Describe the morphology of the erythrocytes.
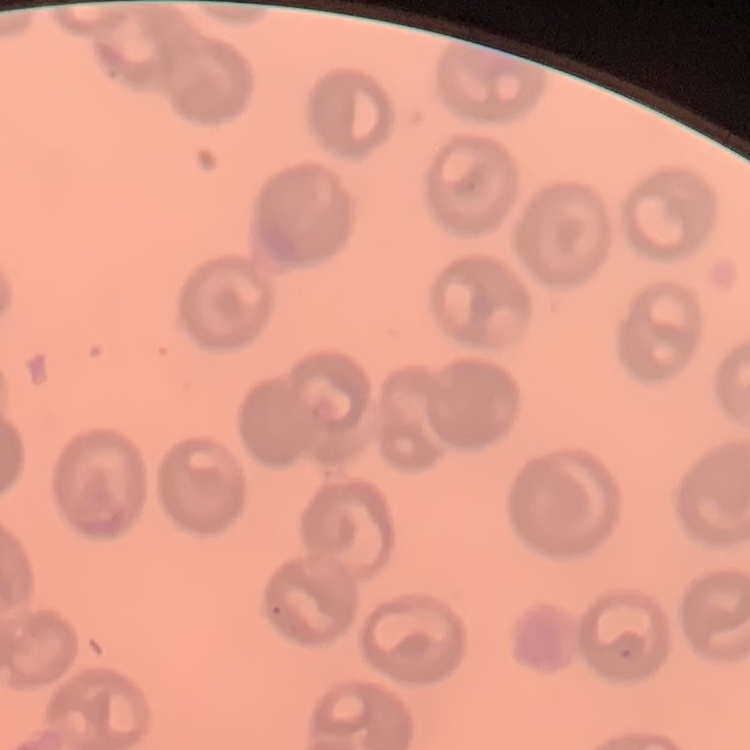
No rouleaux formation.

Thin blood film. Field's or Giemsa stain. Square crop of a larger photomicrograph.